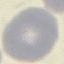 Result: no malaria parasites seen. Acquired by smartphone through the microscope eyepiece. Giemsa stain. Automatically extracted cell patch, resized to 64 × 64 pixels. Thin blood film.